Identify the parasite.
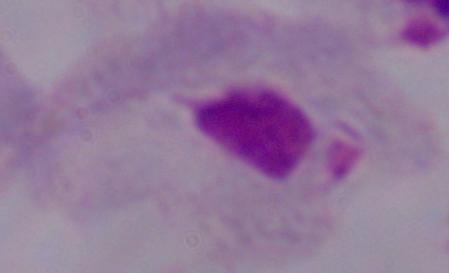
This is a trichomonad.

magnification: 1000x
modality: photomicrograph